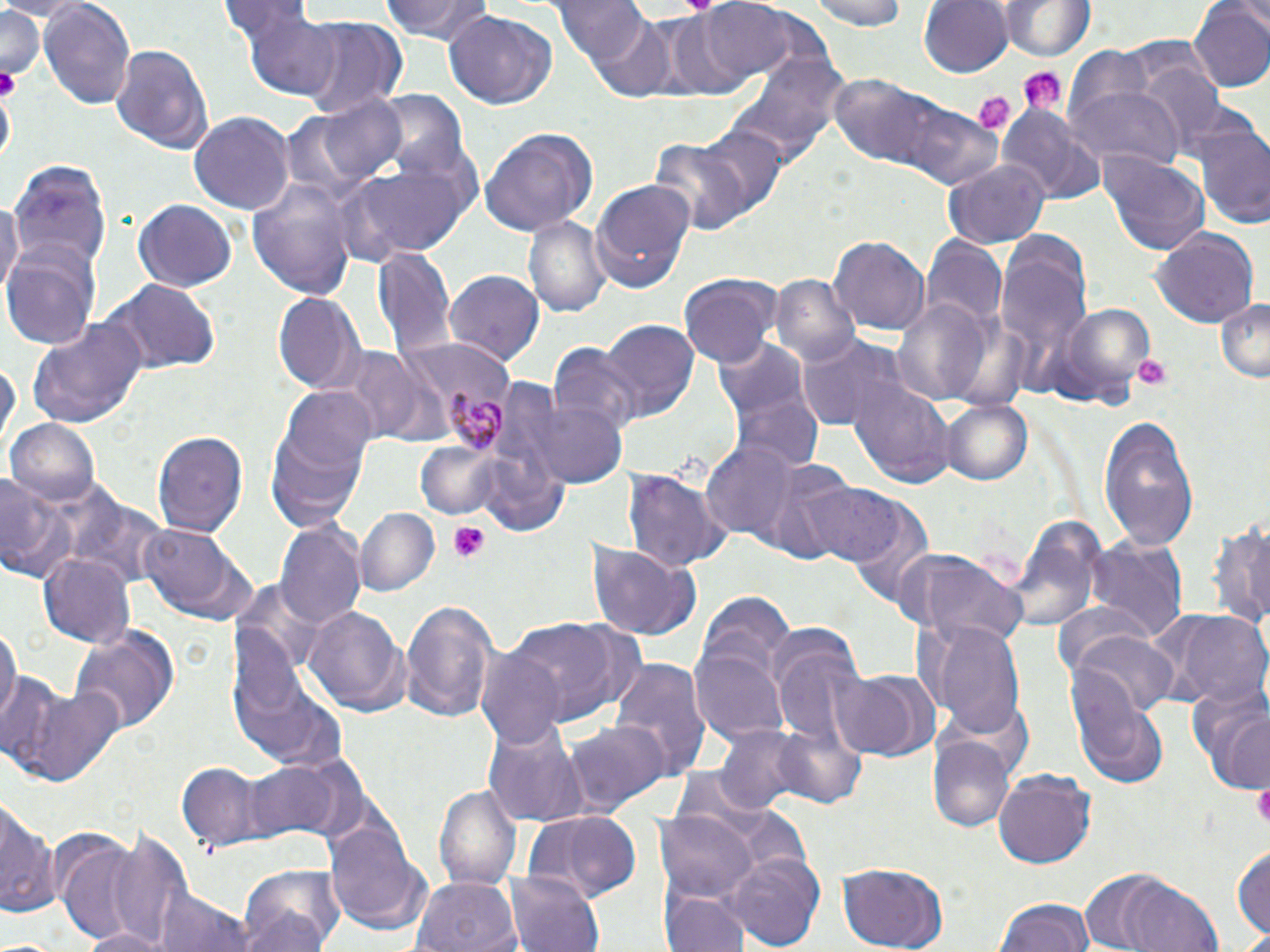
Approximate bounding boxes as (x1, y1, x2, y2) in pixels. Plasmodium malariae-infected red blood cell locations: (438, 383, 511, 453). Uninfected red blood cell locations: (382, 0, 496, 45), (552, 0, 660, 78), (700, 0, 801, 81), (806, 0, 910, 31), (917, 0, 1013, 78), (995, 0, 1097, 60), (39, 1, 136, 113), (1190, 1, 1270, 92), (0, 3, 44, 87), (238, 8, 346, 100), (444, 9, 557, 109), (653, 13, 738, 97), (583, 15, 677, 99), (291, 18, 405, 116), (110, 42, 216, 154), (733, 52, 843, 172), (1131, 59, 1229, 150), (829, 76, 932, 166), (1069, 88, 1182, 170), (290, 93, 411, 196), (374, 93, 468, 183), (885, 96, 1001, 189), (998, 105, 1101, 203), (189, 113, 293, 214), (1192, 118, 1270, 228), (692, 123, 789, 221), (476, 127, 597, 239), (649, 133, 760, 240), (1098, 151, 1211, 258), (348, 160, 472, 256), (945, 160, 1051, 248), (12, 161, 110, 276), (590, 178, 694, 294), (248, 180, 361, 299), (0, 197, 22, 303), (133, 197, 237, 289), (523, 214, 611, 321), (1149, 226, 1259, 329), (829, 235, 930, 336), (3, 239, 102, 350), (922, 239, 1006, 329), (995, 240, 1096, 387), (14, 242, 129, 417), (374, 246, 455, 362), (446, 270, 547, 365), (771, 276, 860, 367), (678, 280, 774, 368), (102, 281, 221, 375), (273, 292, 364, 395), (1213, 294, 1270, 383), (893, 297, 990, 404), (1055, 303, 1155, 404), (27, 316, 149, 428), (595, 321, 698, 422), (799, 336, 903, 433), (715, 337, 826, 473), (548, 343, 643, 438), (331, 346, 433, 444), (1, 356, 17, 452), (849, 378, 956, 486), (279, 387, 376, 483), (525, 395, 627, 489), (937, 396, 1031, 486), (1097, 413, 1197, 550), (264, 414, 368, 531), (6, 418, 100, 505), (153, 427, 248, 540), (702, 440, 800, 538), (416, 443, 498, 519), (475, 444, 574, 535), (756, 461, 861, 568), (622, 468, 729, 573), (0, 472, 72, 585), (801, 482, 902, 568), (58, 489, 170, 587), (835, 489, 932, 602), (355, 508, 440, 596), (1210, 517, 1270, 632), (275, 519, 366, 632), (1008, 519, 1104, 637), (139, 525, 235, 615), (1085, 538, 1187, 641), (584, 540, 700, 641), (39, 551, 135, 647), (904, 556, 1030, 646), (695, 591, 796, 699), (399, 596, 499, 726), (304, 606, 407, 716), (1160, 609, 1270, 707), (504, 616, 644, 723), (1, 620, 18, 730), (928, 621, 1029, 738), (69, 624, 182, 734), (768, 626, 866, 751), (1069, 629, 1178, 720), (691, 644, 790, 746), (476, 645, 567, 748), (609, 658, 711, 781), (831, 666, 939, 762), (4, 676, 124, 791), (1186, 683, 1270, 794), (1072, 685, 1171, 789), (483, 720, 587, 828), (562, 721, 672, 818), (714, 724, 815, 818), (770, 725, 868, 811), (930, 738, 1014, 833), (244, 758, 344, 845), (177, 762, 269, 848), (991, 767, 1098, 870), (434, 781, 520, 887), (0, 791, 57, 921), (657, 808, 756, 903), (526, 810, 641, 900), (327, 818, 427, 930), (48, 826, 164, 946), (106, 828, 196, 947), (1233, 840, 1270, 946), (721, 851, 825, 952), (836, 864, 949, 951), (239, 867, 346, 952), (1077, 867, 1224, 951), (509, 869, 606, 952), (410, 876, 519, 952), (151, 883, 252, 952), (662, 888, 752, 952), (995, 896, 1095, 952), (78, 926, 173, 952). Platelet locations: (1016, 68, 1066, 113), (971, 91, 1012, 134), (1131, 352, 1175, 392), (446, 522, 492, 563), (1253, 781, 1270, 827). Slide-level diagnosis: Plasmodium malariae. Optical microscopy. Thin blood smear. Captured at 1000x magnification. Single field of view. May-Grünwald-Giemsa-stained preparation. Image is 1270×952 pixels.